Locate leukocytes (white blood cells).
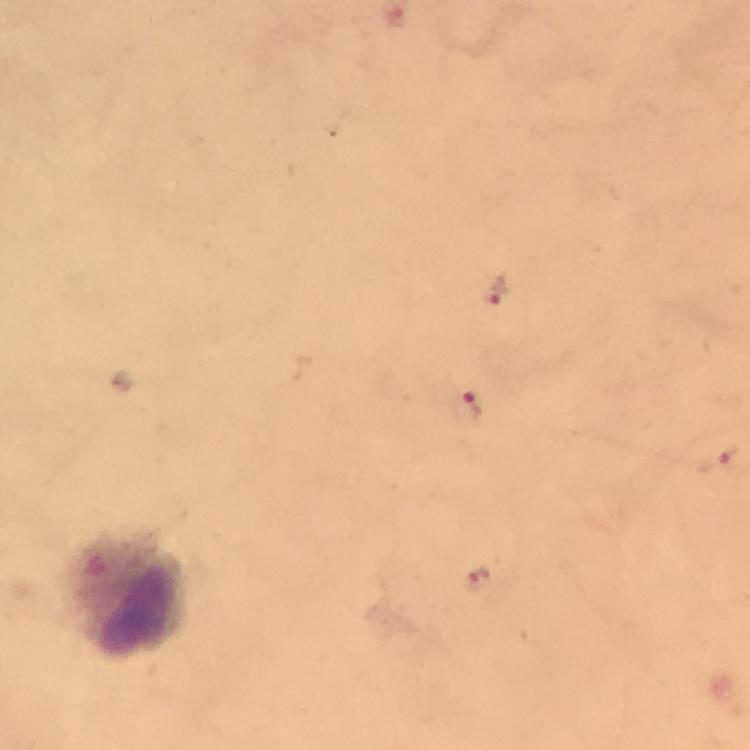

Approximate centers as (x, y) in pixels.
Leukocytes: (128, 596).

immersion_oil: used
image_size: 750×750 pixels
cropped_from: a single field of view
preparation: thick smear
malaria_parasite_locations: 'approximate centers as (x, y) in pixels: (494, 290), (472, 405), (719, 462), (478, 580)'
stain: Giemsa
capture: smartphone mounted on the microscope
context: from a malaria diagnostic workup
magnification: 100x